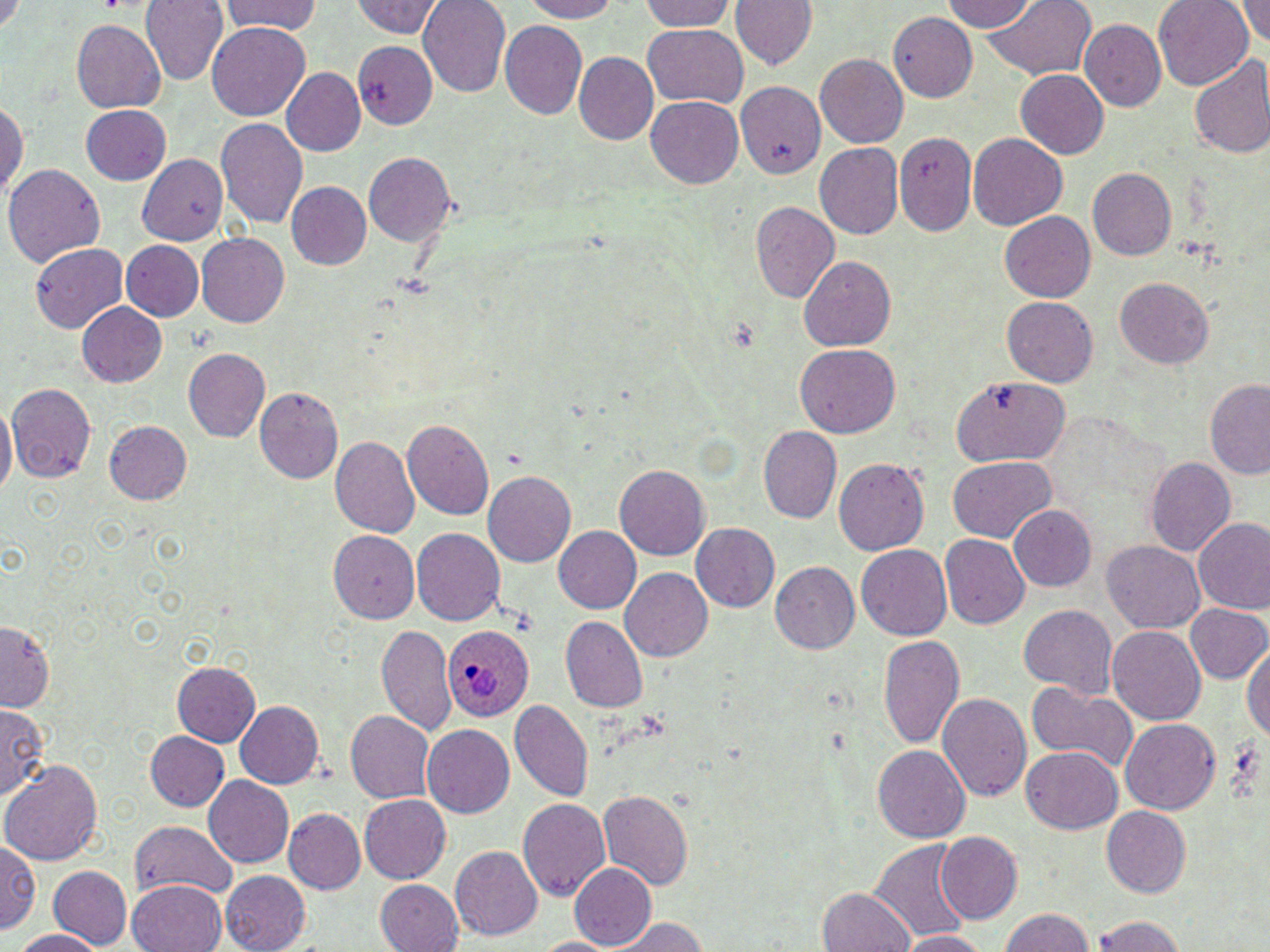

Summary:
  - Coordinate format: approximate bounding boxes as named x1/y1/x2/y2 corners in pixels
  - Uninfected red blood cell locations: (x1=139, y1=0, x2=228, y2=86), (x1=220, y1=0, x2=322, y2=37), (x1=420, y1=0, x2=512, y2=96), (x1=515, y1=0, x2=620, y2=22), (x1=640, y1=0, x2=738, y2=32), (x1=729, y1=0, x2=814, y2=73), (x1=942, y1=0, x2=1042, y2=32), (x1=981, y1=0, x2=1096, y2=82), (x1=1153, y1=0, x2=1253, y2=89), (x1=1234, y1=0, x2=1270, y2=49), (x1=353, y1=1, x2=447, y2=39), (x1=889, y1=12, x2=979, y2=101), (x1=1077, y1=16, x2=1165, y2=109), (x1=71, y1=19, x2=166, y2=113), (x1=207, y1=22, x2=310, y2=121), (x1=500, y1=22, x2=588, y2=121), (x1=642, y1=25, x2=747, y2=108), (x1=352, y1=41, x2=436, y2=129), (x1=574, y1=54, x2=658, y2=144), (x1=816, y1=54, x2=908, y2=147), (x1=1188, y1=55, x2=1270, y2=160), (x1=282, y1=68, x2=366, y2=155), (x1=1014, y1=69, x2=1109, y2=160), (x1=735, y1=82, x2=823, y2=178), (x1=645, y1=94, x2=744, y2=186), (x1=0, y1=95, x2=27, y2=207), (x1=80, y1=105, x2=171, y2=184), (x1=216, y1=117, x2=309, y2=231), (x1=891, y1=131, x2=972, y2=234), (x1=968, y1=133, x2=1067, y2=229), (x1=815, y1=142, x2=903, y2=239), (x1=362, y1=153, x2=457, y2=248), (x1=136, y1=154, x2=229, y2=248), (x1=5, y1=161, x2=105, y2=269), (x1=1087, y1=169, x2=1177, y2=262), (x1=284, y1=182, x2=370, y2=271), (x1=751, y1=204, x2=839, y2=302), (x1=999, y1=210, x2=1098, y2=302), (x1=196, y1=233, x2=289, y2=328), (x1=122, y1=240, x2=204, y2=319), (x1=31, y1=241, x2=130, y2=332), (x1=798, y1=256, x2=896, y2=351), (x1=1116, y1=277, x2=1215, y2=370), (x1=1002, y1=296, x2=1097, y2=388), (x1=74, y1=300, x2=166, y2=388), (x1=796, y1=345, x2=900, y2=438), (x1=183, y1=348, x2=271, y2=441), (x1=947, y1=375, x2=1069, y2=466), (x1=1204, y1=378, x2=1270, y2=480), (x1=6, y1=383, x2=97, y2=483), (x1=254, y1=385, x2=342, y2=482), (x1=0, y1=403, x2=16, y2=503), (x1=401, y1=417, x2=495, y2=520), (x1=100, y1=418, x2=196, y2=505), (x1=758, y1=427, x2=842, y2=522), (x1=330, y1=436, x2=420, y2=540), (x1=1146, y1=455, x2=1236, y2=558), (x1=834, y1=456, x2=929, y2=553), (x1=948, y1=456, x2=1055, y2=545), (x1=613, y1=464, x2=709, y2=560), (x1=484, y1=473, x2=577, y2=568), (x1=1008, y1=505, x2=1097, y2=593), (x1=1192, y1=517, x2=1270, y2=617), (x1=691, y1=523, x2=780, y2=613), (x1=551, y1=526, x2=640, y2=614), (x1=328, y1=529, x2=419, y2=624), (x1=411, y1=529, x2=505, y2=626), (x1=942, y1=535, x2=1032, y2=628), (x1=1104, y1=538, x2=1204, y2=632), (x1=856, y1=545, x2=954, y2=641), (x1=770, y1=563, x2=861, y2=657), (x1=619, y1=567, x2=713, y2=662), (x1=1185, y1=604, x2=1270, y2=685), (x1=1019, y1=605, x2=1117, y2=700), (x1=559, y1=615, x2=647, y2=714), (x1=0, y1=620, x2=55, y2=710), (x1=377, y1=622, x2=453, y2=735), (x1=1107, y1=626, x2=1205, y2=725), (x1=878, y1=634, x2=963, y2=747), (x1=1242, y1=640, x2=1270, y2=749), (x1=172, y1=661, x2=260, y2=745), (x1=1025, y1=680, x2=1138, y2=775), (x1=939, y1=691, x2=1033, y2=803), (x1=233, y1=701, x2=323, y2=790), (x1=509, y1=701, x2=592, y2=802), (x1=0, y1=706, x2=47, y2=804), (x1=344, y1=711, x2=434, y2=804), (x1=1121, y1=718, x2=1220, y2=814), (x1=421, y1=725, x2=515, y2=819), (x1=145, y1=731, x2=229, y2=811), (x1=872, y1=745, x2=968, y2=843), (x1=1021, y1=747, x2=1122, y2=833), (x1=1, y1=758, x2=102, y2=867), (x1=201, y1=776, x2=293, y2=869), (x1=598, y1=789, x2=693, y2=890), (x1=357, y1=794, x2=451, y2=884), (x1=517, y1=798, x2=610, y2=905), (x1=1102, y1=807, x2=1191, y2=897), (x1=282, y1=809, x2=366, y2=896), (x1=129, y1=819, x2=238, y2=902), (x1=934, y1=833, x2=1022, y2=925), (x1=871, y1=838, x2=974, y2=942), (x1=0, y1=839, x2=40, y2=938), (x1=451, y1=847, x2=544, y2=941), (x1=567, y1=861, x2=656, y2=950), (x1=50, y1=866, x2=132, y2=947), (x1=220, y1=871, x2=311, y2=952), (x1=375, y1=878, x2=463, y2=952), (x1=128, y1=879, x2=228, y2=952), (x1=817, y1=886, x2=915, y2=952), (x1=999, y1=906, x2=1097, y2=952), (x1=1088, y1=915, x2=1188, y2=952), (x1=612, y1=917, x2=713, y2=952), (x1=8, y1=930, x2=108, y2=952), (x1=895, y1=931, x2=995, y2=951), (x1=532, y1=934, x2=621, y2=951)
  - Plasmodium ovale-infected red blood cell locations: (x1=441, y1=626, x2=532, y2=721)
  - Slide-level diagnosis: Plasmodium ovale
  - Magnification: 1000x
  - Stain: May-Grünwald-Giemsa
  - Preparation: thin blood smear
  - Modality: optical microscopy
  - Field of view: one of a larger specimen
  - Image size: 1270×952 pixels